Point out each Plasmodium parasite.
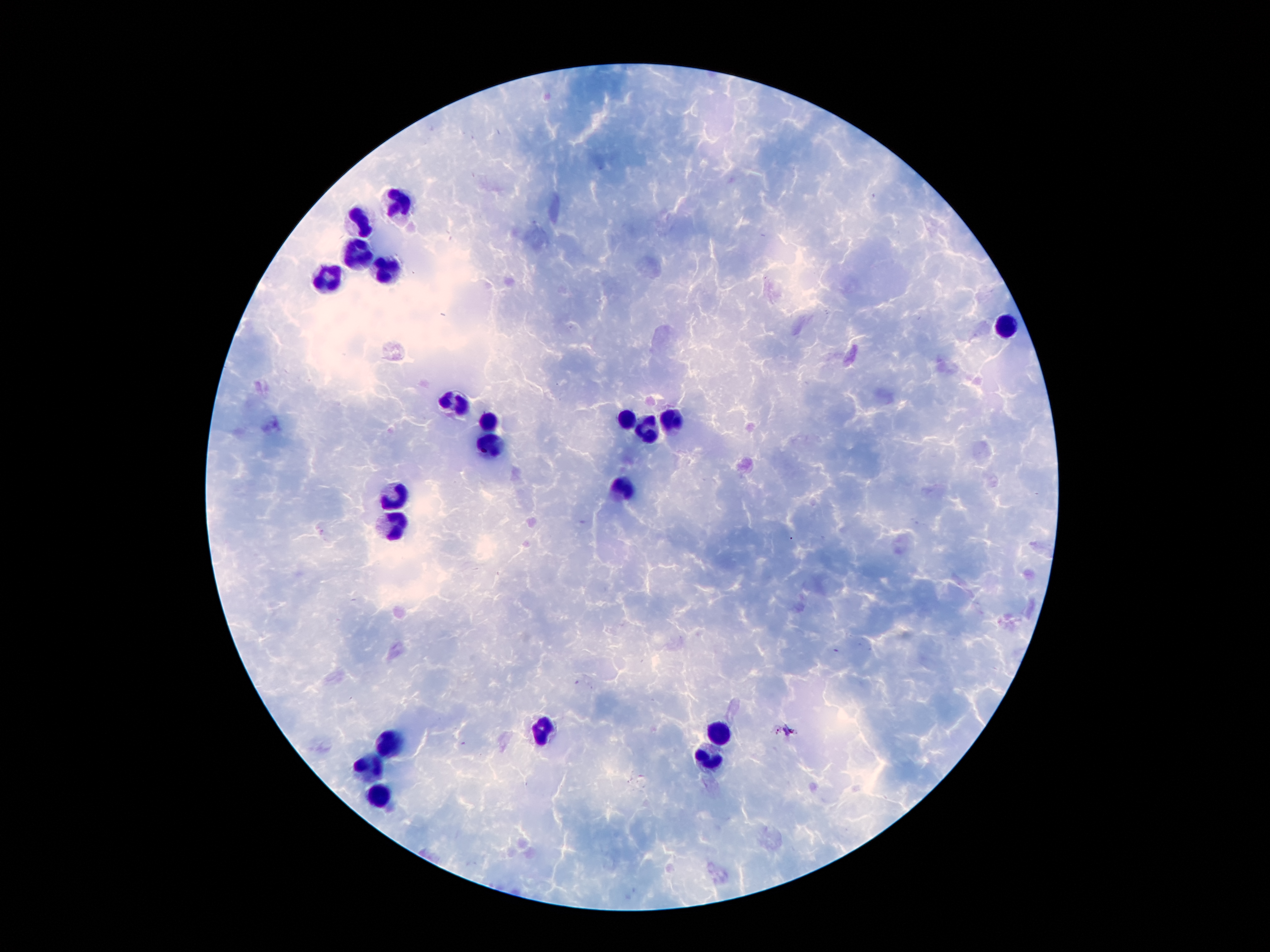
Approximate object centers, in pixels from the top-left corner.
Plasmodium parasites: (x=789, y=730).

Summary:
  - Leukocyte locations: (x=397, y=203), (x=357, y=221), (x=355, y=253), (x=389, y=271), (x=325, y=277), (x=1005, y=325), (x=453, y=403), (x=629, y=419), (x=671, y=419), (x=489, y=425), (x=647, y=433), (x=493, y=449), (x=623, y=491), (x=391, y=497), (x=395, y=527), (x=539, y=727), (x=721, y=731), (x=389, y=745), (x=711, y=759), (x=367, y=771), (x=379, y=797)
  - Preparation: thick blood film
  - Patient malaria status: infected with Plasmodium falciparum
  - Image size: 1270×952 pixels
  - Stain: Giemsa
  - Magnification: 100x
  - Capture: smartphone camera through the microscope eyepiece
  - Field of view: one from this slide